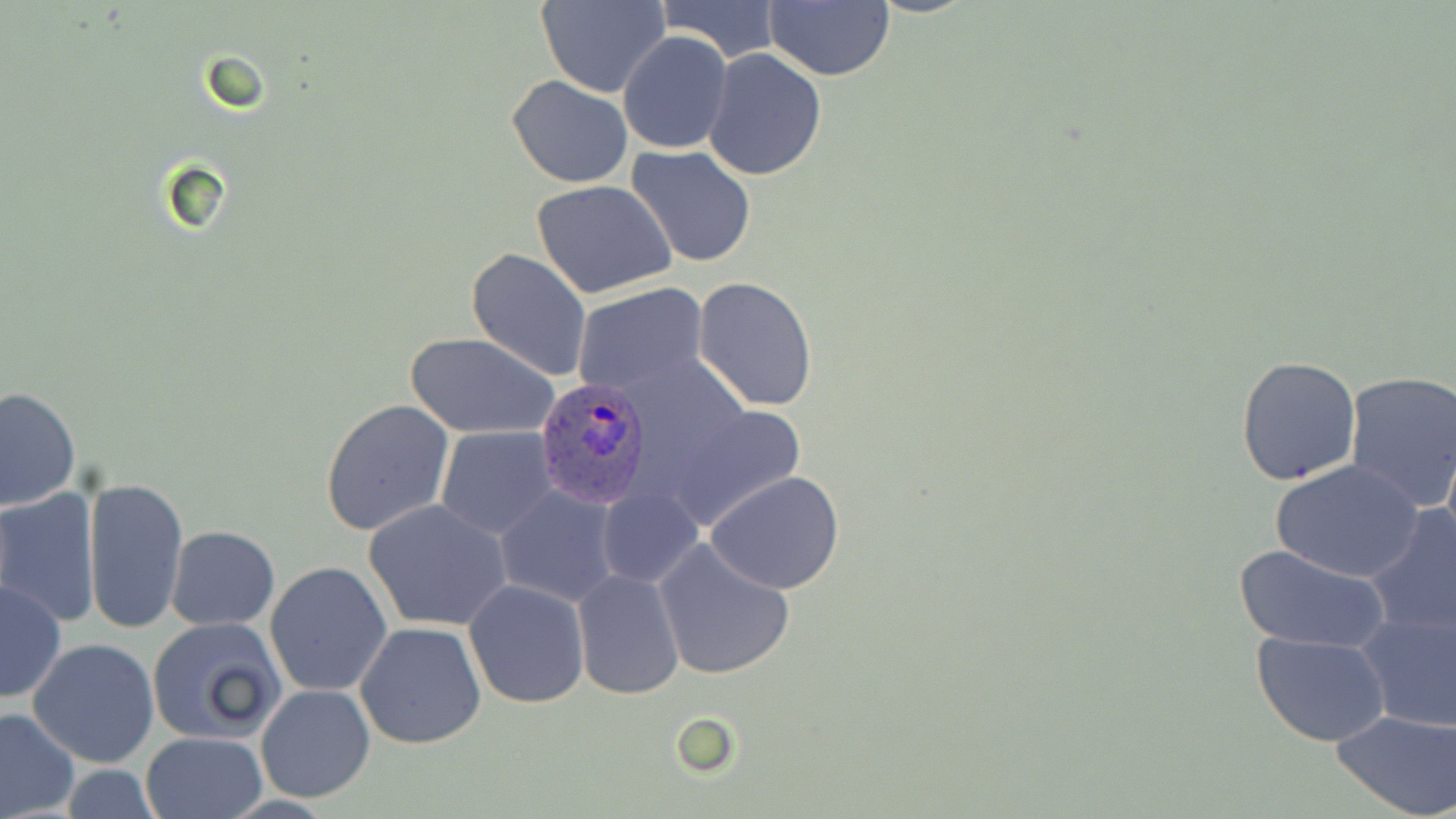

Summary:
  - Coordinate format: approximate bounding boxes as (x1,y1)-(x2,y2) corner pairs in pixels
  - Uninfected red blood cell locations: (537,0)-(671,98), (652,0)-(784,64), (764,0)-(893,82), (866,0)-(980,18), (618,30)-(733,154), (701,46)-(828,180), (506,76)-(633,187), (626,145)-(757,270), (532,179)-(679,300), (466,247)-(593,381), (694,277)-(818,412), (572,283)-(709,397), (405,332)-(560,439), (1235,355)-(1362,486), (1343,370)-(1456,513), (0,387)-(80,510), (320,399)-(454,536), (669,403)-(808,531), (434,425)-(559,539), (1272,459)-(1423,583), (705,470)-(846,593), (83,476)-(189,635), (494,485)-(622,607), (596,486)-(702,589), (0,488)-(102,628), (362,498)-(514,633), (1363,505)-(1456,640), (166,526)-(279,630), (654,538)-(796,683), (1233,543)-(1390,652), (265,562)-(392,696), (572,569)-(684,700), (1,579)-(67,706), (465,579)-(590,709), (1352,604)-(1456,732), (147,616)-(287,745), (356,622)-(488,750), (1252,632)-(1389,747), (29,638)-(159,768), (256,684)-(375,802), (0,707)-(79,818), (1333,709)-(1455,818), (140,732)-(267,818)
  - Plasmodium ovale-infected red blood cell locations: (537,378)-(653,509)
  - Slide-level diagnosis: Plasmodium ovale
  - Preparation: thin blood film
  - Field of view: single
  - Stain: May-Grünwald-Giemsa
  - Modality: light microscopy
  - Image size: 1456×819 pixels
  - Magnification: 1000x